Assess this cell for malaria.
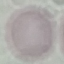

It is uninfected.

Summary:
  - Image type: automatically extracted cell patch, resized to 64 × 64 pixels
  - Preparation: thin blood smear
  - Capture: smartphone camera at the microscope eyepiece
  - Stain: Giemsa